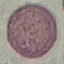
Summary:
  - Result: negative for malaria parasites
  - Preparation: thin blood film
  - Capture: smartphone camera at the microscope eyepiece
  - Image type: automatically extracted cell patch, resized to 64 × 64 pixels
  - Stain: Giemsa